Identify the cell.
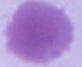

This is an erythrocyte.

magnification = 1000x
modality = photomicrograph